Locate and identify every blood parasite.
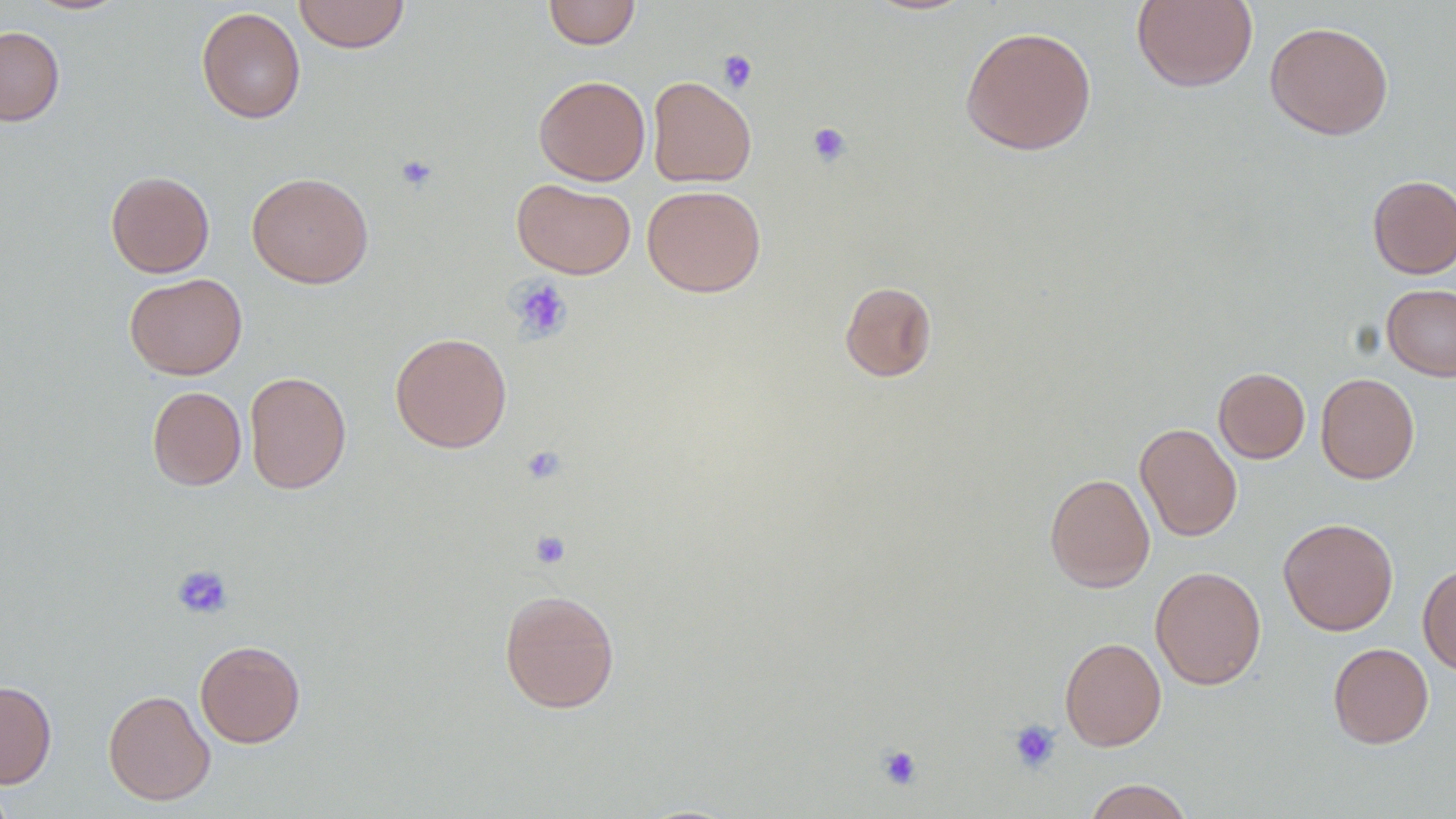
No blood parasites observed.

Approximate bounding boxes as (x1,y1)-(x2,y2) corner pairs in pixels. Uninfected red blood cell locations: (21,0)-(133,16), (293,0)-(411,54), (543,0)-(641,49), (1131,0)-(1258,93), (196,7)-(306,124), (1264,21)-(1393,140), (0,26)-(65,126), (959,26)-(1097,155), (533,75)-(650,185), (647,76)-(757,187), (105,171)-(214,277), (247,172)-(373,288), (1367,174)-(1456,279), (512,179)-(636,278), (642,184)-(766,297), (124,273)-(247,379), (839,281)-(937,382), (1382,284)-(1456,381), (389,332)-(512,453), (1213,367)-(1310,463), (244,371)-(351,494), (1315,372)-(1419,483), (147,386)-(246,491), (1135,423)-(1242,541), (1044,472)-(1155,592), (1278,517)-(1398,635), (1418,563)-(1456,674), (1150,565)-(1266,690), (498,588)-(620,714), (1059,637)-(1167,751), (195,640)-(305,748), (1328,643)-(1434,748), (0,680)-(57,787), (103,689)-(215,805), (0,775)-(18,819), (1082,779)-(1195,819). Platelet locations: (718,49)-(758,93), (807,122)-(852,167), (394,154)-(439,193), (509,277)-(574,342), (520,445)-(567,485), (531,530)-(571,569), (172,564)-(233,620), (1008,719)-(1062,774), (877,744)-(923,790). Slide-level diagnosis: no evidence of blood parasites. Optical microscopy. Captured at 1000x magnification. Thin blood film. Single field of view. Image is 1456×819 pixels.